State the preparation type.
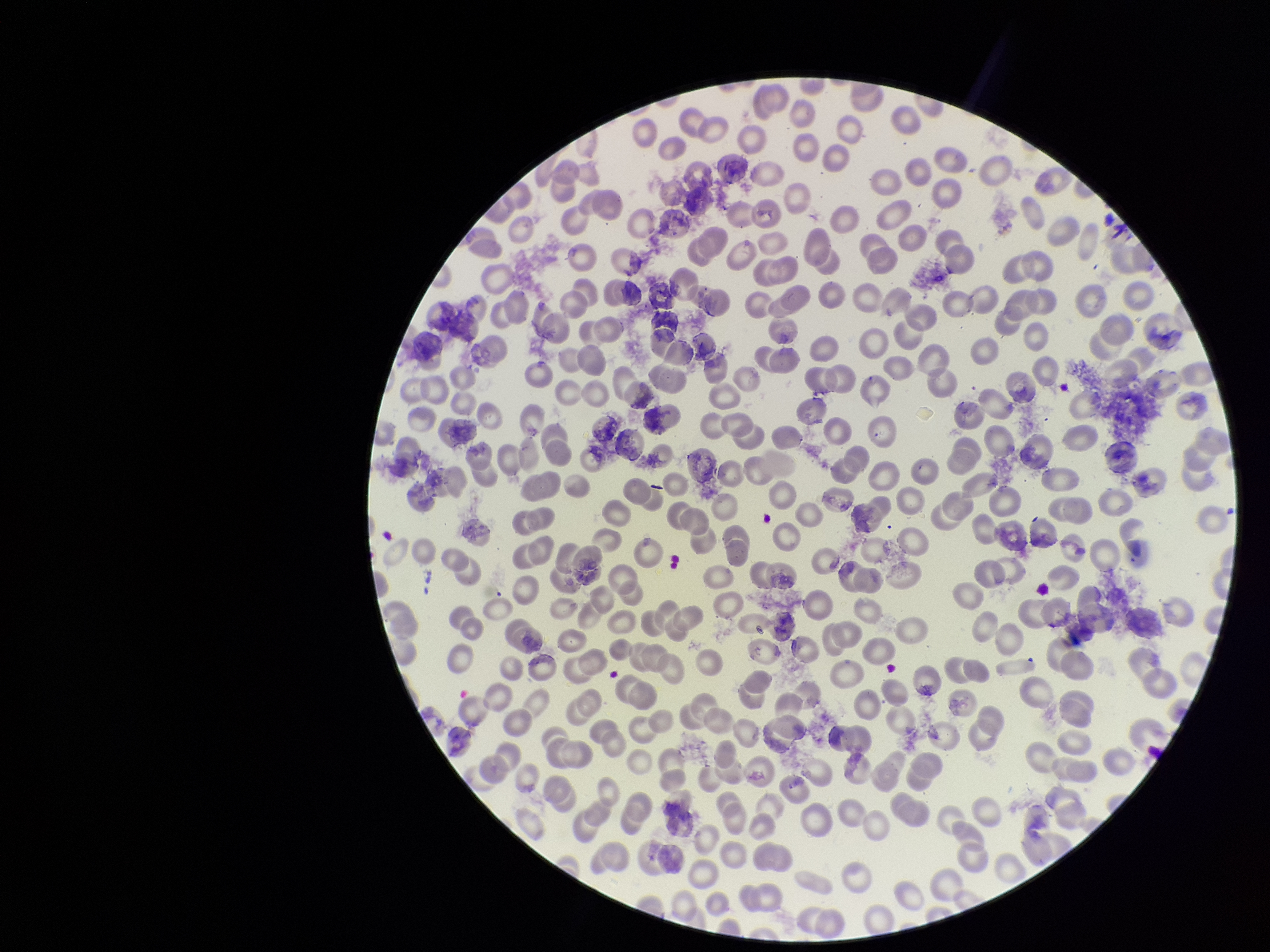
A thin smear.

{
  "parasitized_red_blood_cell_count": 0,
  "parasitized_red_blood_cells": "none identified",
  "capture": "smartphone photograph through the microscope eyepiece",
  "image_size": "1270×952 pixels",
  "red_blood_cell_count": 269,
  "field_of_view": "one from this slide",
  "patient_malaria_status": "negative",
  "stain": "Giemsa"
}